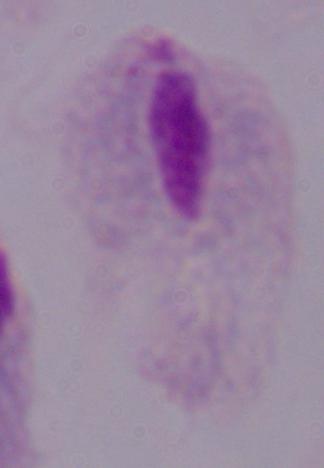

{
  "magnification": "1000x",
  "identification": "trichomonad",
  "modality": "photomicrograph"
}